Give a bounding box for every parasitised red blood cell, every trophozoite, every gametocyte, every leukocyte, and every artifact (platelet-like body, stain precipitate, or debris).
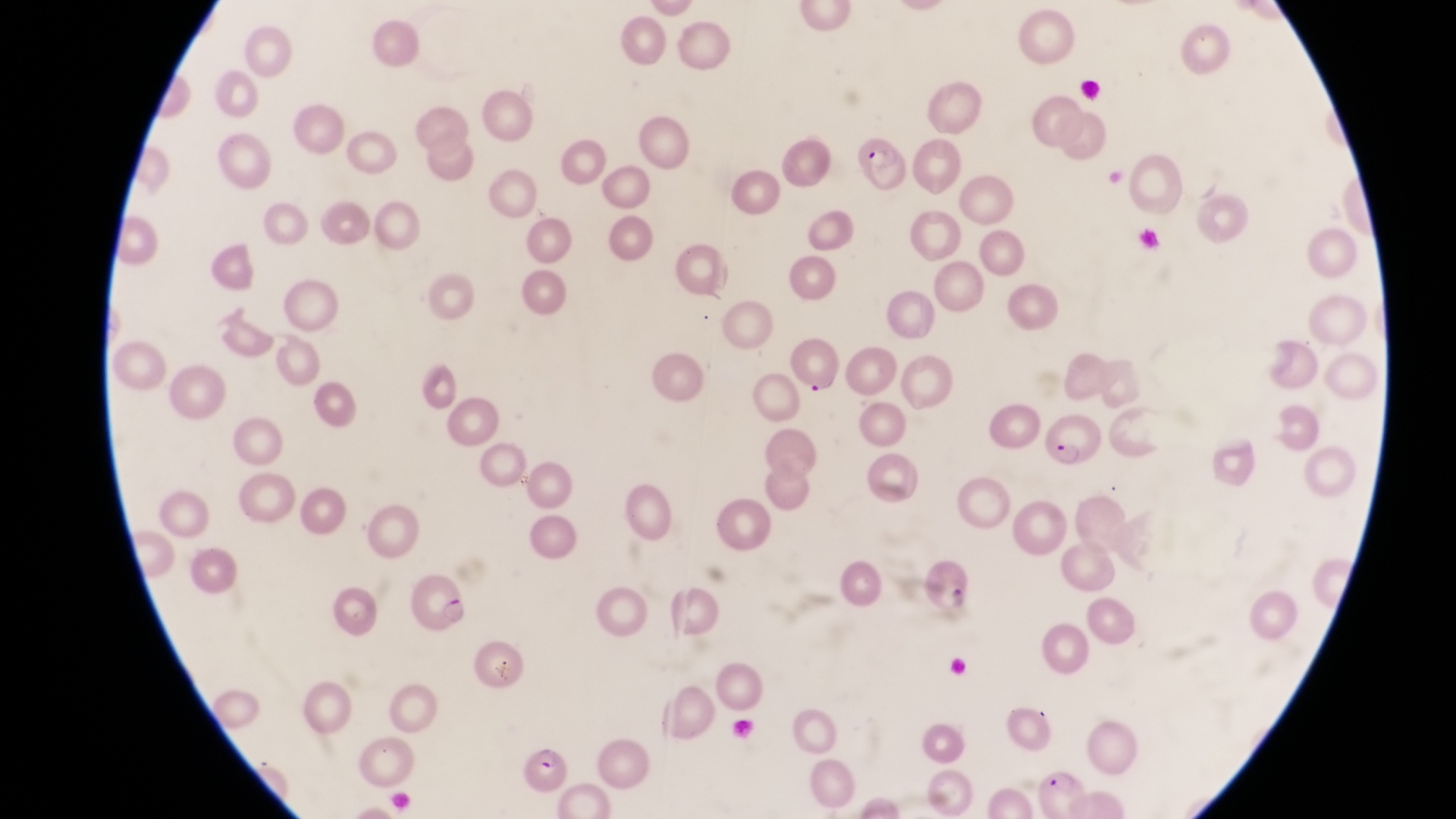

Approximate bounding boxes as (left, top, right, bottom) in pixels.
Parasitised red blood cells: (854, 130, 910, 186), (785, 331, 845, 394), (1044, 406, 1115, 489), (406, 576, 469, 636), (522, 745, 567, 797), (1037, 770, 1093, 817).
No leukocytes observed.

Magnification of 1000x. Image is 1456×819 pixels. Captured by a smartphone held over the eyepiece of an Olympus CX-23 microscope. Single field of view. Sample from Uganda. Thin blood smear.